Classify this cell by malaria status.
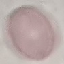
It is uninfected.

Summary:
  - Capture: smartphone through the microscope eyepiece
  - Stain: Giemsa
  - Image type: automatically extracted cell patch, resized to 64 × 64 pixels
  - Preparation: thin blood smear